Report the malaria status of this cell.
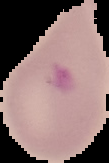

It is parasitized.

preparation = thin blood smear
image type = segmented cell region with the area outside set to black
image size = 109×163 pixels